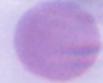

Summary:
  - Magnification: 1000x
  - Identification: erythrocyte
  - Modality: micrograph